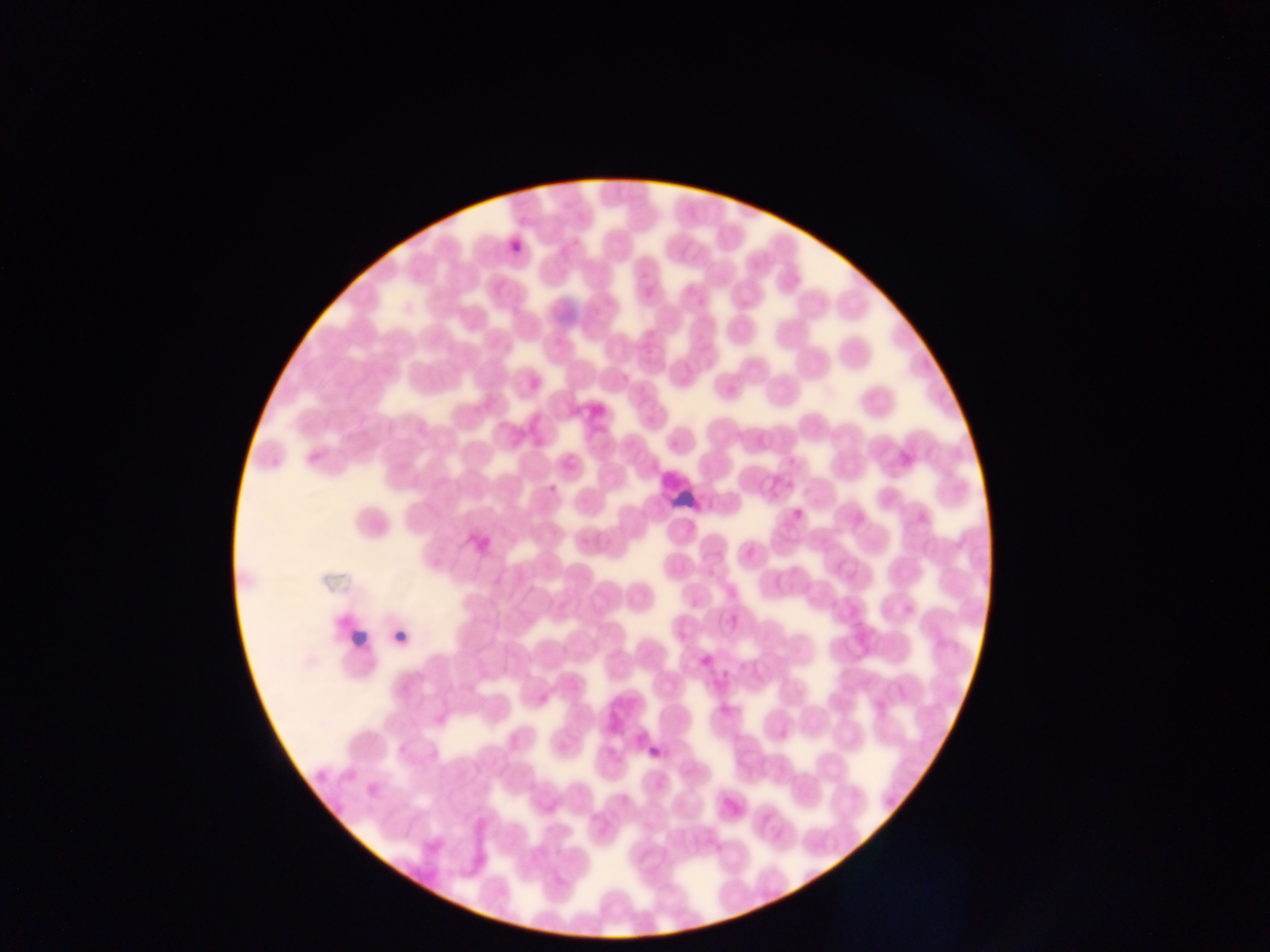
Approximate bounding boxes as left top right bottom in pixels.
Summary:
  - Leukocyte locations: 668 484 698 512; 346 628 366 658
  - Malaria parasite locations: 509 225 535 250; 545 479 560 496; 393 627 410 650; 646 743 669 765
  - Image size: 1270×952 pixels
  - Capture: mobile-phone photograph through a microscope
  - Field of view: single
  - Country: Ghana
  - Preparation: thin blood smear